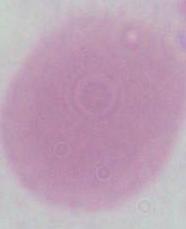

Summary:
  - Identification: red blood cell
  - Magnification: 1000x
  - Modality: photomicrograph